Report the malaria status of this cell.
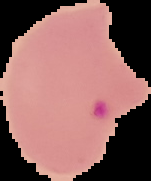

Parasitized.

Image is 151×181 pixels. Cell region segmented out of the field of view; the surrounding area is masked to black. From a thin blood film.